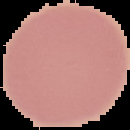
{
  "image_size": "130×130 pixels",
  "image_type": "segmented cell region on a black background",
  "preparation": "thin blood film",
  "result": "no Plasmodium parasites detected"
}